Classify this cell by malaria status.
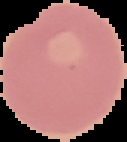
It is uninfected.

The area outside the segmented cell region is set to black. Image is 127×142 pixels. From a thin blood film.